Report the malaria status of this cell.
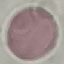
It is uninfected.

Summary:
  - Image type: cell patch, automatically extracted from a larger field of view and resized to 64 × 64 pixels
  - Preparation: thin blood film
  - Capture: smartphone camera at the microscope eyepiece
  - Stain: Giemsa